State which parasite is depicted.
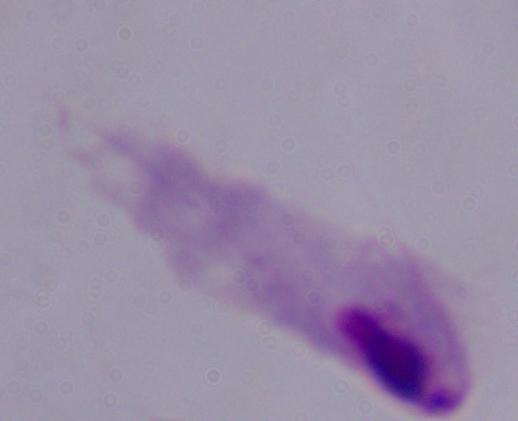

A trichomonad.

Micrograph. Captured at 1000x magnification.